Give the preparation type.
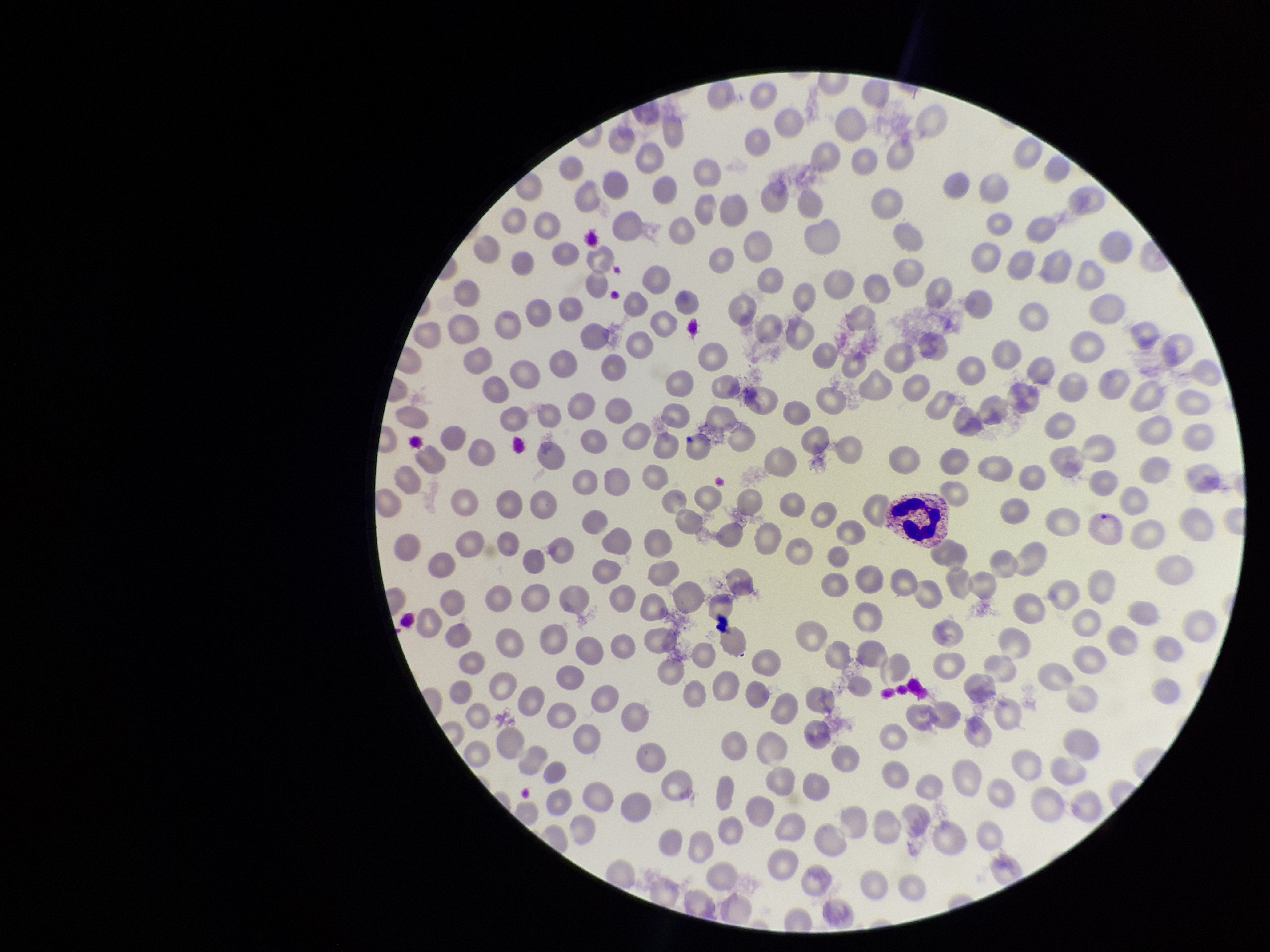

Thin.

parasitized red blood cells = detected
parasitized red blood cell count = 1
stain = Giemsa
field of view = one from this slide
image size = 1270×952 pixels
red blood cell count = 274
capture = smartphone photograph through the microscope eyepiece
species reported for this patient = Plasmodium vivax
patient malaria status = positive